Report the malaria status of this cell.
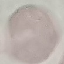

It is uninfected.

Summary:
  - Capture: smartphone through the microscope eyepiece
  - Preparation: thin smear
  - Stain: Giemsa
  - Image type: cell patch, automatically extracted from a larger field of view and resized to 64 × 64 pixels